Give the position of every Plasmodium parasite visible.
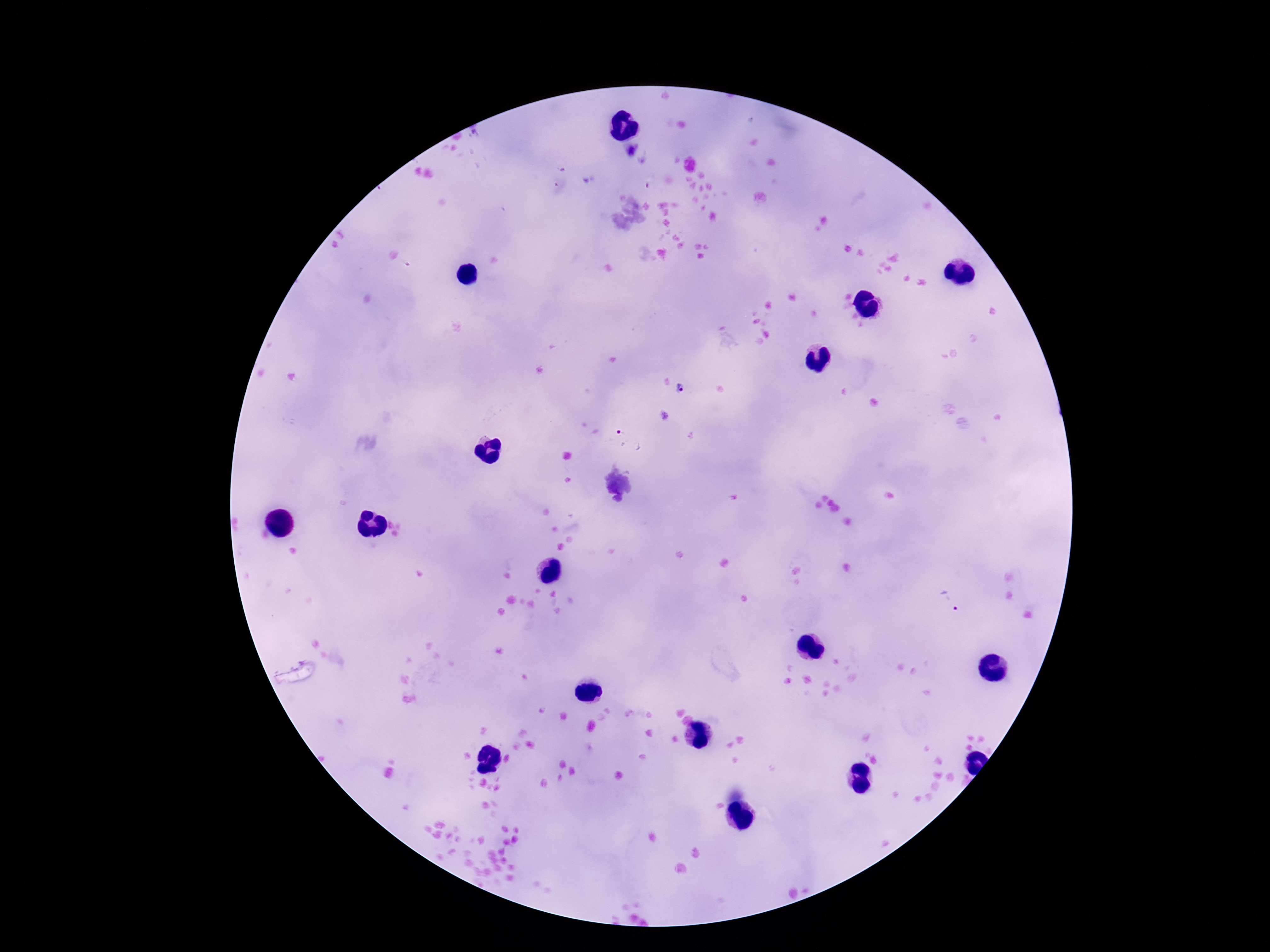

Approximate centers as {x, y} in pixels.
Plasmodium parasites: {631, 149}, {680, 389}, {629, 439}, {951, 603}.

Single field of view. Image is 1270×952 pixels. Smartphone photograph taken through the microscope eyepiece. Giemsa-stained preparation. 100x magnification. Patient malaria status: positive. Thick blood film.